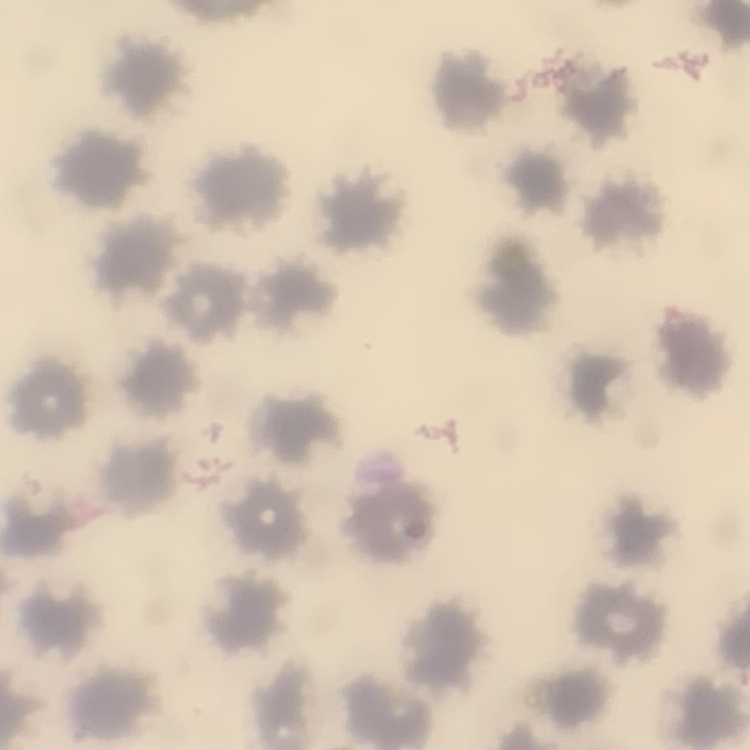 The erythrocytes show no rouleaux formation. Field's or Giemsa stain. Thin blood smear. Square crop of a larger photomicrograph.